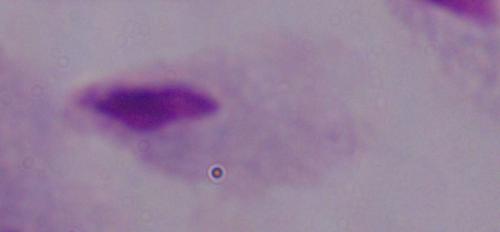
magnification: 1000x
identification: trichomonad
modality: micrograph